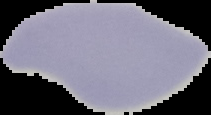

Summary:
  - Malaria status: uninfected
  - Image size: 211×115 pixels
  - Image type: segmented cell region with the area outside set to black
  - Preparation: thin blood film